Comment on the morphology of the red blood cells.
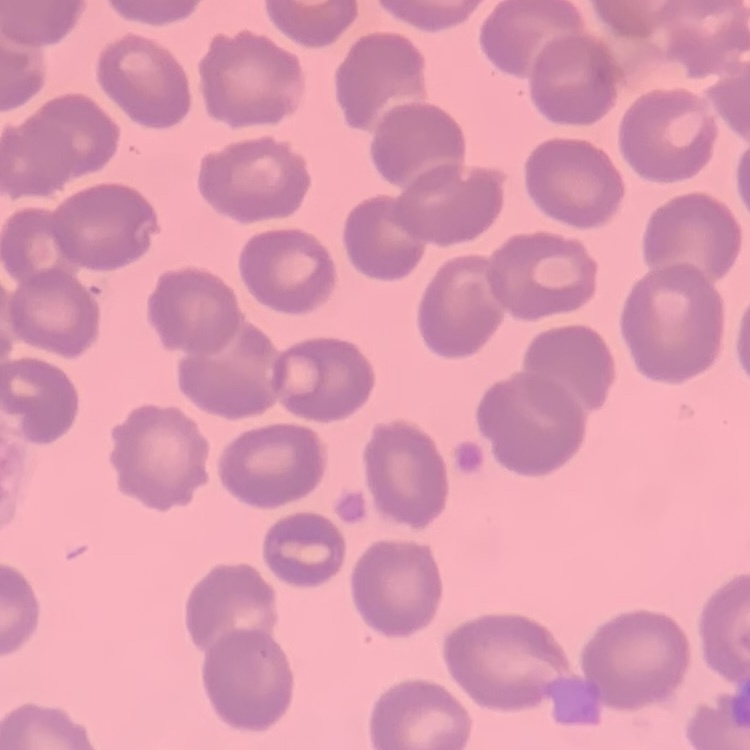
No rouleaux formation.

One tile cut from a larger photomicrograph. Stained with either Field's or Giemsa. Thin blood smear.